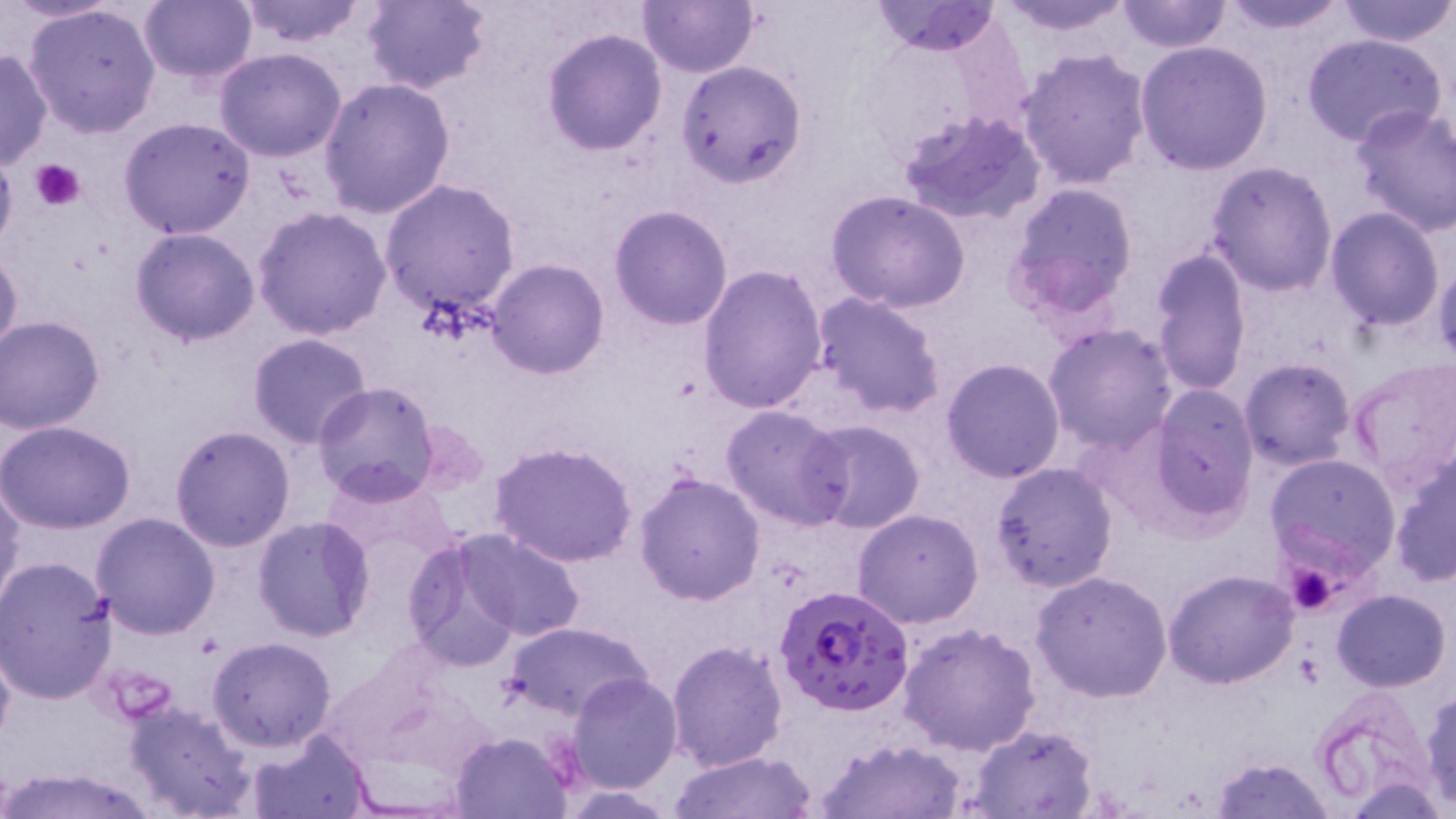
slide_level_diagnosis: Plasmodium falciparum
image_size: 1456×819 pixels
magnification: 1000x
modality: optical microscopy
stain: May-Grünwald-Giemsa
field_of_view: single
preparation: thin blood film
plasmodium_falciparum_infected_red_blood_cell_locations: 'approximate bounding boxes as [x1, y1, x2, y2] in pixels: [776, 585, 915, 716]'
platelet_locations: 'approximate bounding boxes as [x1, y1, x2, y2] in pixels: [32, 159, 85, 211], [1283, 565, 1344, 616]'
uninfected_red_blood_cell_locations: 'approximate bounding boxes as [x1, y1, x2, y2] in pixels: [234, 0, 369, 48], [359, 0, 492, 94], [638, 0, 761, 77], [871, 0, 1003, 53], [996, 0, 1140, 37], [1113, 0, 1234, 54], [1214, 0, 1352, 35], [138, 1, 258, 85], [1335, 1, 1456, 46], [24, 2, 163, 139], [542, 28, 668, 154], [1301, 33, 1446, 148], [1134, 40, 1276, 176], [0, 47, 52, 172], [213, 47, 348, 163], [1017, 47, 1153, 191], [160, 56, 316, 199], [676, 58, 806, 185], [318, 76, 458, 218], [1349, 103, 1456, 238], [900, 107, 1047, 226], [116, 116, 257, 240], [0, 149, 19, 257], [1206, 160, 1339, 295], [379, 180, 522, 320], [1004, 181, 1141, 318], [825, 191, 971, 314], [609, 204, 733, 330], [251, 205, 393, 341], [1324, 206, 1446, 331], [131, 228, 261, 346], [0, 244, 23, 365], [1148, 244, 1254, 396], [1433, 254, 1456, 368], [486, 259, 609, 379], [698, 265, 828, 415], [811, 291, 948, 419], [0, 316, 104, 433], [1044, 323, 1178, 452], [247, 332, 374, 448], [940, 357, 1067, 483], [1239, 358, 1357, 470], [1345, 360, 1456, 494], [312, 382, 440, 504], [1146, 385, 1260, 523], [720, 404, 852, 530], [800, 417, 927, 534], [0, 420, 136, 533], [168, 424, 295, 551], [489, 441, 638, 567], [1390, 452, 1455, 587], [1265, 453, 1402, 574], [988, 461, 1119, 594], [324, 472, 456, 578], [634, 473, 766, 607], [0, 477, 24, 612], [852, 508, 985, 628], [91, 514, 221, 640], [252, 516, 377, 642], [452, 529, 587, 641], [401, 533, 526, 670], [0, 556, 119, 704], [1162, 569, 1300, 689], [1031, 571, 1173, 703], [1332, 588, 1451, 692], [503, 620, 652, 722], [898, 621, 1042, 756], [207, 636, 337, 753], [0, 639, 16, 753], [665, 639, 788, 773], [567, 672, 683, 792], [1421, 688, 1456, 809], [124, 697, 256, 818], [965, 722, 1099, 817], [448, 729, 576, 818], [245, 731, 374, 817], [818, 738, 969, 818], [670, 749, 815, 819], [1210, 757, 1336, 819], [0, 768, 158, 819]'